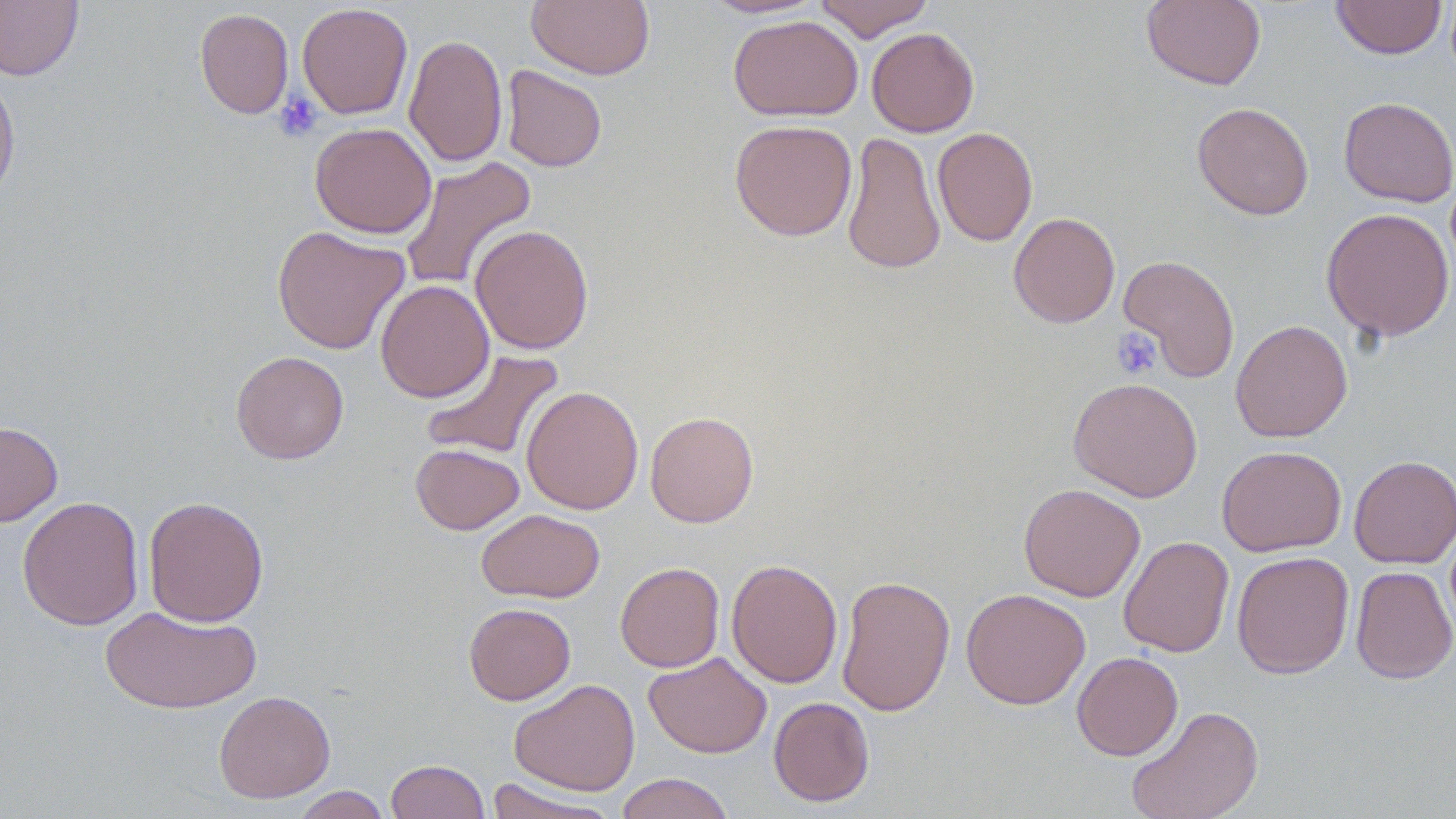

Approximate bounding boxes as (x1,y1)-(x2,y2) corner pairs in pixels. Uninfected red blood cell locations: (0,0)-(83,81), (526,0)-(655,80), (699,0)-(827,19), (813,0)-(934,41), (1141,0)-(1266,90), (1331,0)-(1448,60), (297,2)-(413,119), (194,8)-(294,119), (728,15)-(863,121), (866,27)-(979,137), (404,34)-(508,168), (501,65)-(607,172), (0,71)-(20,205), (1338,96)-(1456,207), (1192,102)-(1314,220), (729,119)-(857,242), (310,122)-(436,239), (932,127)-(1038,246), (842,131)-(945,276), (398,157)-(538,293), (1321,207)-(1455,341), (1008,212)-(1120,328), (470,224)-(594,354), (272,225)-(410,355), (1118,254)-(1240,382), (375,279)-(494,402), (1230,320)-(1353,442), (420,348)-(564,461), (231,351)-(349,464), (1068,377)-(1203,502), (522,385)-(644,514), (645,411)-(759,527), (0,420)-(62,527), (411,443)-(524,534), (1216,445)-(1347,556), (1349,455)-(1456,568), (1018,483)-(1145,601), (17,496)-(144,630), (143,496)-(269,627), (476,509)-(605,603), (1118,536)-(1234,657), (1232,550)-(1354,678), (726,558)-(843,689), (615,562)-(724,672), (1350,565)-(1456,684), (836,574)-(956,716), (961,587)-(1090,709), (464,603)-(575,705), (100,605)-(260,715), (644,651)-(772,759), (1072,651)-(1183,761), (508,678)-(640,796), (213,690)-(335,803), (768,696)-(874,806), (1126,705)-(1264,819), (385,759)-(490,819), (615,772)-(735,819), (485,778)-(619,819), (291,786)-(392,818). Platelet locations: (273,92)-(323,142), (1111,327)-(1162,380). Slide-level diagnosis: negative for blood parasites. Optical microscopy. 1000x magnification. May-Grünwald-Giemsa-stained preparation. Image is 1456×819 pixels. Thin blood film. One field of a larger specimen.